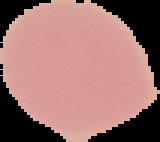 The area outside the segmented cell region is set to black. Image is 160×142 pixels. Result: no Plasmodium parasites seen. From a thin blood smear.